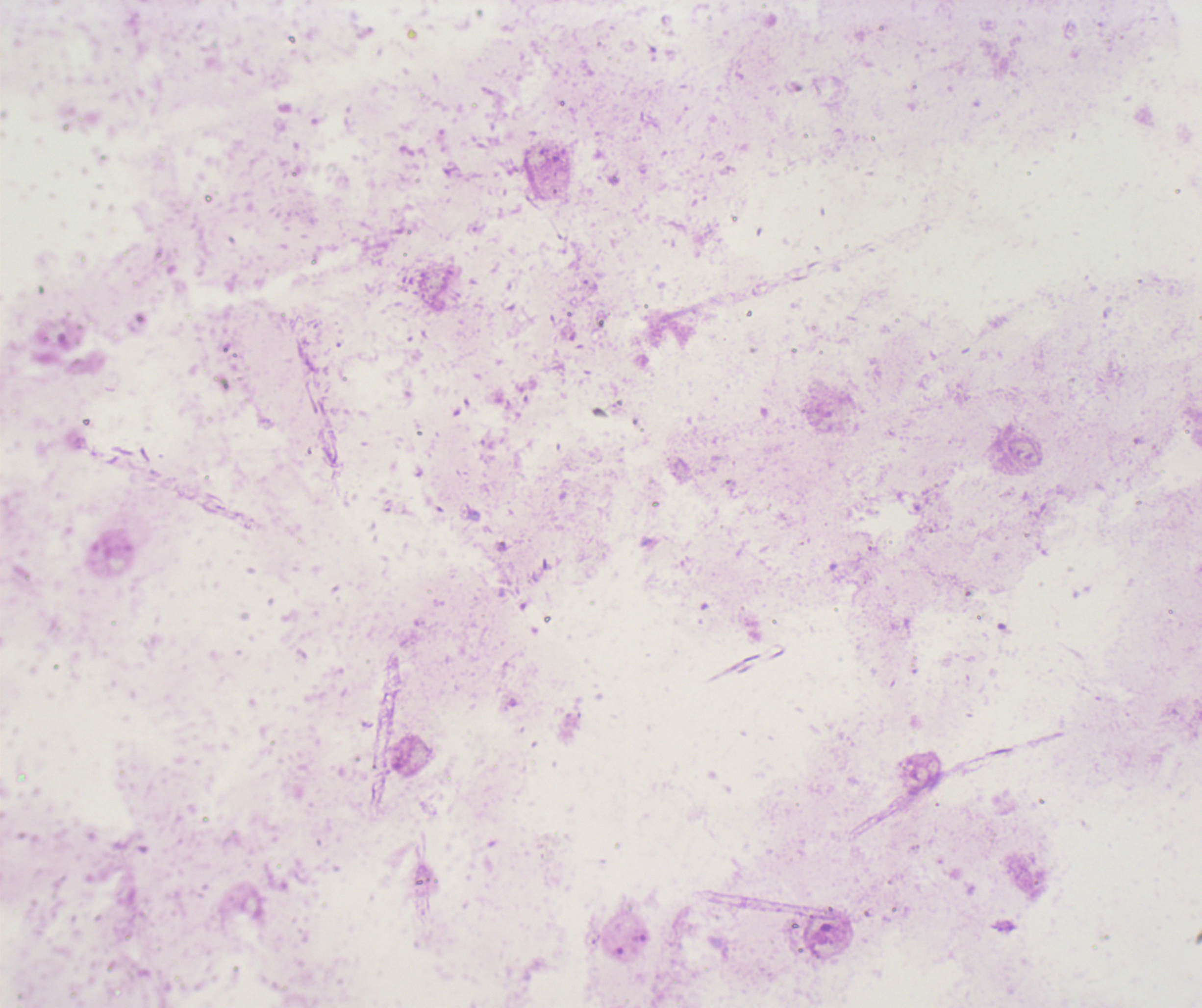

Approximate centers as {x, y} in pixels. Trophozoite locations: {639, 937}. Leukocytes: none visible. Captured at 100x magnification. Image is 1202×1008 pixels. Thick blood smear. One field from this slide. Background quality: unsatisfactory. Romanowsky stain. Result: Plasmodium parasites detected. Previously used in an actual diagnosis. Coloration quality: bad.